Name the parasite shown.
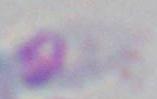

This is Toxoplasma gondii.

Summary:
  - Modality: micrograph
  - Magnification: 1000x